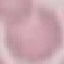
result = no malaria parasites detected
image type = cell patch, automatically extracted from a larger field of view and resized to 64 × 64 pixels
preparation = thin blood smear
stain = Giemsa
capture = smartphone camera at the microscope eyepiece